Name the blood parasite species.
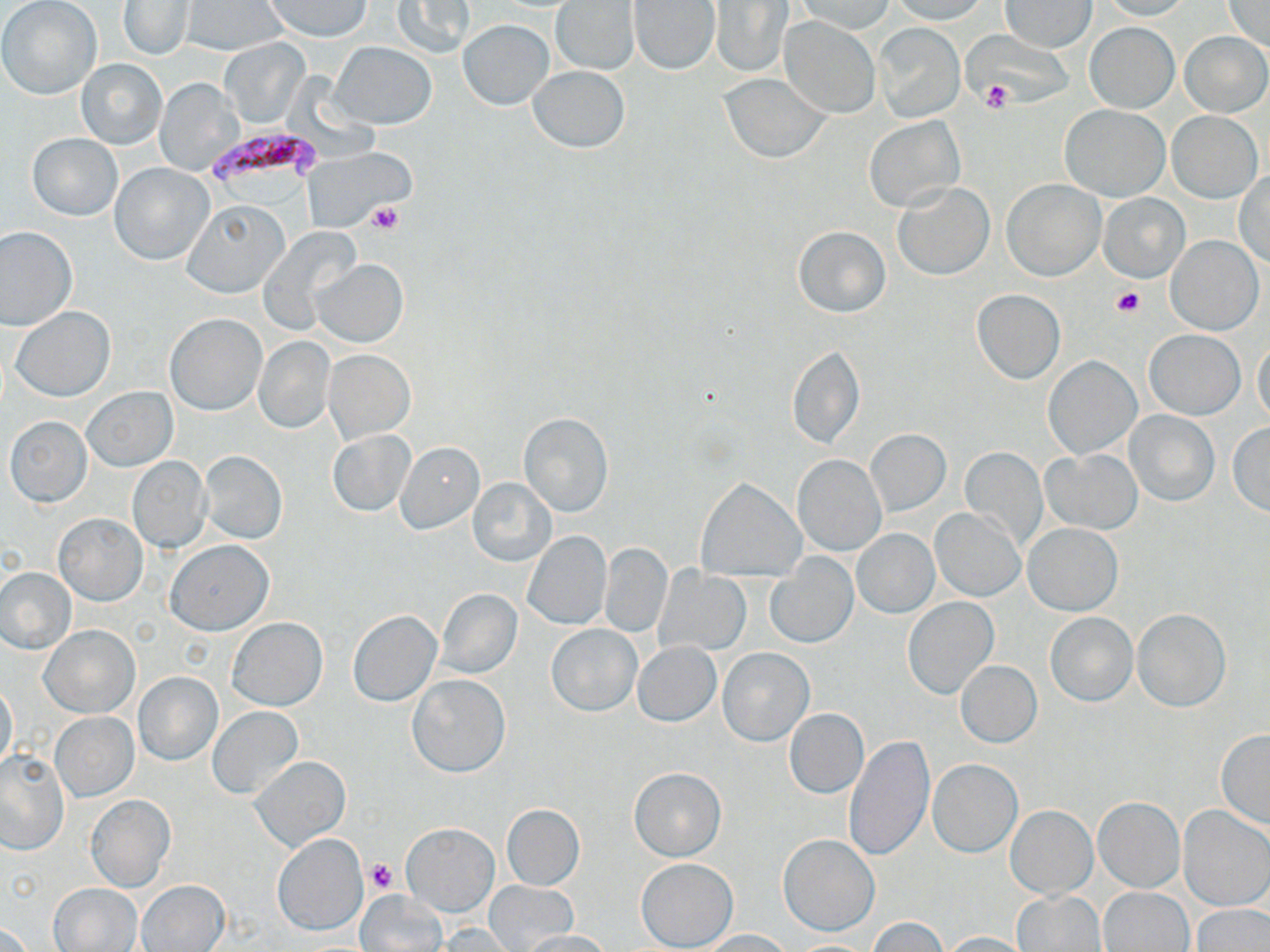
Plasmodium falciparum.

Summary:
  - Coordinate format: approximate bounding boxes as named x1/y1/x2/y2 corners in pixels
  - Uninfected red blood cell locations: (x1=265, y1=0, x2=370, y2=40), (x1=393, y1=0, x2=475, y2=58), (x1=552, y1=0, x2=639, y2=74), (x1=794, y1=0, x2=895, y2=33), (x1=888, y1=0, x2=991, y2=24), (x1=1223, y1=0, x2=1270, y2=50), (x1=1, y1=1, x2=102, y2=101), (x1=709, y1=1, x2=792, y2=75), (x1=1000, y1=1, x2=1095, y2=51), (x1=1098, y1=1, x2=1192, y2=22), (x1=119, y1=2, x2=194, y2=60), (x1=181, y1=2, x2=286, y2=55), (x1=629, y1=2, x2=720, y2=74), (x1=780, y1=17, x2=880, y2=119), (x1=457, y1=19, x2=555, y2=110), (x1=1086, y1=22, x2=1178, y2=111), (x1=871, y1=24, x2=964, y2=123), (x1=1181, y1=32, x2=1269, y2=117), (x1=221, y1=38, x2=309, y2=128), (x1=331, y1=41, x2=435, y2=128), (x1=76, y1=58, x2=167, y2=149), (x1=527, y1=66, x2=631, y2=152), (x1=719, y1=73, x2=830, y2=162), (x1=155, y1=79, x2=242, y2=174), (x1=1061, y1=105, x2=1169, y2=201), (x1=1166, y1=111, x2=1263, y2=203), (x1=864, y1=115, x2=964, y2=212), (x1=28, y1=133, x2=122, y2=221), (x1=305, y1=149, x2=414, y2=229), (x1=110, y1=163, x2=214, y2=265), (x1=1234, y1=172, x2=1270, y2=268), (x1=1003, y1=179, x2=1104, y2=280), (x1=894, y1=183, x2=994, y2=281), (x1=1099, y1=194, x2=1189, y2=282), (x1=183, y1=199, x2=288, y2=297), (x1=0, y1=226, x2=77, y2=330), (x1=794, y1=226, x2=890, y2=318), (x1=259, y1=227, x2=361, y2=333), (x1=1165, y1=235, x2=1263, y2=334), (x1=312, y1=259, x2=408, y2=346), (x1=972, y1=289, x2=1065, y2=384), (x1=11, y1=305, x2=114, y2=401), (x1=164, y1=313, x2=265, y2=416), (x1=1145, y1=329, x2=1246, y2=420), (x1=1251, y1=336, x2=1269, y2=427), (x1=254, y1=337, x2=335, y2=432), (x1=787, y1=343, x2=864, y2=451), (x1=324, y1=349, x2=415, y2=443), (x1=1044, y1=356, x2=1141, y2=458), (x1=82, y1=386, x2=177, y2=472), (x1=1124, y1=410, x2=1219, y2=506), (x1=518, y1=413, x2=613, y2=517), (x1=5, y1=416, x2=91, y2=507), (x1=1227, y1=422, x2=1270, y2=515), (x1=866, y1=429, x2=951, y2=516), (x1=328, y1=431, x2=414, y2=516), (x1=396, y1=442, x2=483, y2=533), (x1=959, y1=447, x2=1048, y2=549), (x1=1044, y1=449, x2=1143, y2=535), (x1=198, y1=450, x2=287, y2=544), (x1=793, y1=455, x2=886, y2=555), (x1=127, y1=456, x2=211, y2=553), (x1=467, y1=479, x2=555, y2=565), (x1=698, y1=479, x2=804, y2=581), (x1=931, y1=507, x2=1025, y2=601), (x1=54, y1=514, x2=146, y2=605), (x1=1023, y1=523, x2=1123, y2=615), (x1=852, y1=529, x2=939, y2=618), (x1=522, y1=531, x2=611, y2=629), (x1=166, y1=541, x2=273, y2=636), (x1=600, y1=543, x2=672, y2=637), (x1=768, y1=557, x2=859, y2=648), (x1=1, y1=566, x2=75, y2=653), (x1=654, y1=566, x2=751, y2=656), (x1=436, y1=589, x2=523, y2=678), (x1=903, y1=597, x2=999, y2=698), (x1=1133, y1=608, x2=1230, y2=711), (x1=347, y1=610, x2=443, y2=707), (x1=1046, y1=612, x2=1137, y2=706), (x1=227, y1=618, x2=327, y2=710), (x1=547, y1=624, x2=641, y2=716), (x1=41, y1=625, x2=140, y2=718), (x1=634, y1=642, x2=721, y2=727), (x1=718, y1=648, x2=814, y2=745), (x1=955, y1=660, x2=1042, y2=747), (x1=133, y1=671, x2=222, y2=765), (x1=407, y1=675, x2=510, y2=777), (x1=0, y1=683, x2=18, y2=773), (x1=208, y1=706, x2=303, y2=801), (x1=784, y1=708, x2=869, y2=799), (x1=49, y1=713, x2=138, y2=801), (x1=1215, y1=730, x2=1270, y2=829), (x1=843, y1=735, x2=935, y2=863), (x1=1, y1=751, x2=67, y2=854), (x1=250, y1=754, x2=350, y2=852), (x1=927, y1=759, x2=1022, y2=857), (x1=628, y1=767, x2=726, y2=860), (x1=85, y1=795, x2=175, y2=892), (x1=1093, y1=797, x2=1184, y2=893), (x1=503, y1=804, x2=584, y2=889), (x1=1005, y1=806, x2=1097, y2=897), (x1=1179, y1=806, x2=1270, y2=910), (x1=402, y1=822, x2=499, y2=916), (x1=272, y1=832, x2=367, y2=936), (x1=778, y1=834, x2=879, y2=935), (x1=635, y1=857, x2=738, y2=951), (x1=137, y1=880, x2=230, y2=951), (x1=485, y1=881, x2=576, y2=951), (x1=49, y1=882, x2=143, y2=951), (x1=1101, y1=887, x2=1193, y2=951), (x1=356, y1=890, x2=446, y2=952), (x1=1013, y1=890, x2=1105, y2=952), (x1=1193, y1=905, x2=1270, y2=952), (x1=867, y1=917, x2=948, y2=951), (x1=0, y1=923, x2=33, y2=952), (x1=434, y1=923, x2=519, y2=950), (x1=697, y1=929, x2=792, y2=951), (x1=519, y1=930, x2=614, y2=952), (x1=940, y1=931, x2=1036, y2=951)
  - Platelet locations: (x1=980, y1=79, x2=1013, y2=113), (x1=364, y1=202, x2=403, y2=235), (x1=1112, y1=287, x2=1145, y2=317), (x1=365, y1=858, x2=400, y2=893)
  - Plasmodium falciparum-infected red blood cell locations: (x1=205, y1=126, x2=323, y2=195)
  - Preparation: thin blood smear
  - Modality: light microscopy
  - Magnification: 1000x
  - Field of view: one of a larger specimen
  - Image size: 1270×952 pixels
  - Stain: May-Grünwald-Giemsa